Outline each blood parasite and name the species.
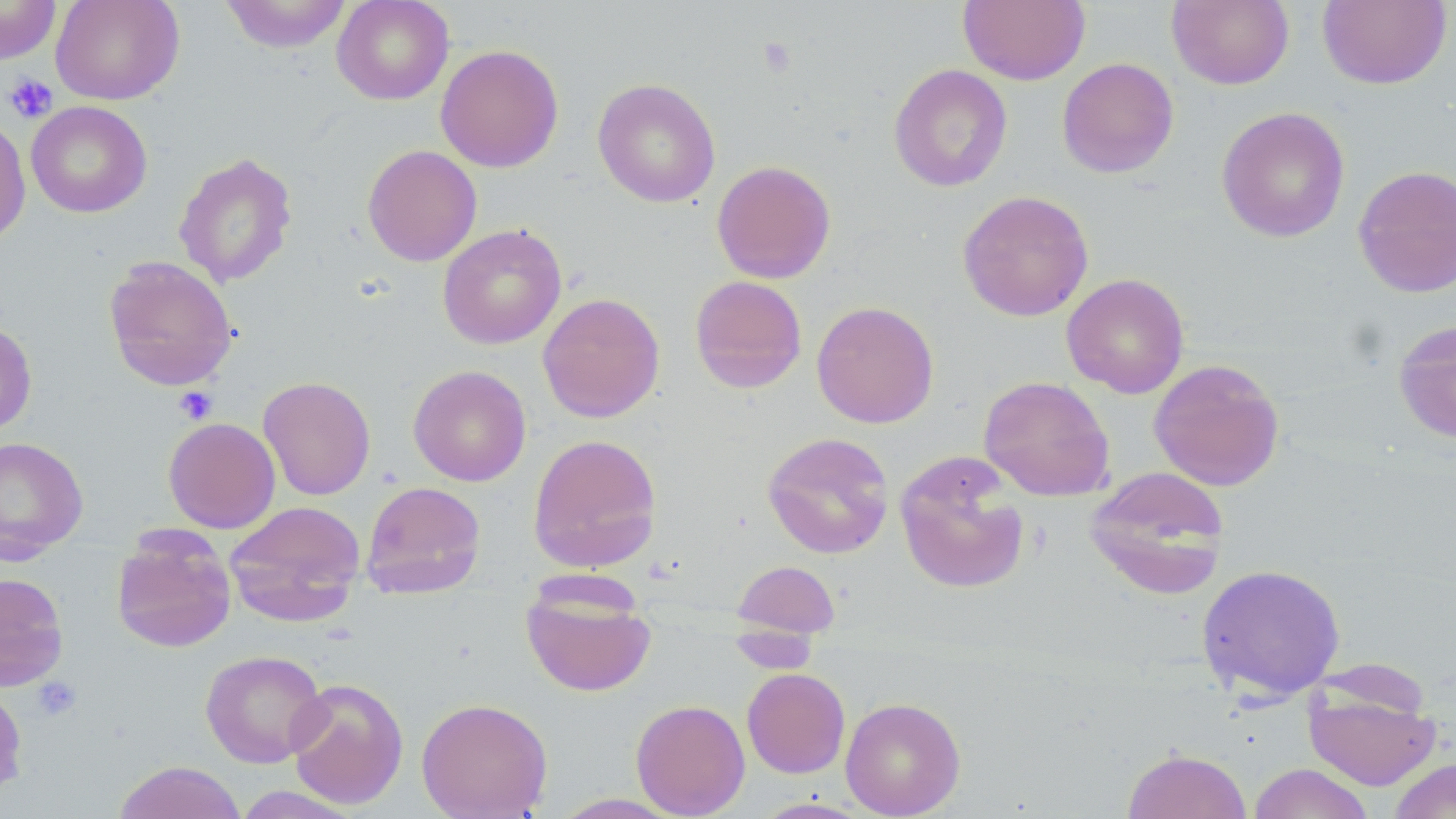
No blood parasites observed.

Approximate bounding boxes as (x1, y1, x2, y2) in pixels. Uninfected red blood cell locations: (0, 0, 62, 65), (50, 0, 184, 105), (220, 0, 353, 53), (332, 0, 454, 105), (958, 0, 1090, 86), (1318, 0, 1451, 89), (1167, 1, 1294, 90), (435, 44, 564, 172), (1056, 57, 1179, 179), (888, 64, 1013, 192), (592, 78, 721, 207), (26, 100, 152, 218), (1216, 106, 1350, 243), (0, 113, 31, 249), (362, 144, 483, 267), (173, 152, 298, 288), (711, 160, 836, 284), (1352, 165, 1456, 298), (957, 190, 1094, 322), (438, 224, 566, 349), (103, 256, 238, 392), (1062, 273, 1189, 399), (689, 275, 808, 393), (537, 292, 665, 423), (811, 301, 939, 428), (0, 319, 37, 437), (1393, 319, 1456, 444), (1148, 358, 1285, 491), (408, 365, 531, 487), (258, 375, 376, 501), (978, 376, 1115, 501), (163, 417, 280, 533), (762, 432, 895, 559), (527, 433, 662, 573), (0, 437, 89, 564), (895, 453, 1030, 595), (1086, 467, 1231, 600), (360, 480, 486, 599), (225, 500, 366, 625), (111, 528, 236, 653), (733, 560, 840, 638), (1196, 563, 1345, 701), (0, 572, 69, 691), (520, 578, 656, 697), (729, 635, 820, 671), (200, 649, 328, 768), (742, 668, 850, 778), (286, 677, 409, 810), (0, 681, 28, 800), (1304, 684, 1440, 790), (415, 696, 553, 819), (840, 696, 966, 818), (631, 699, 750, 818), (1121, 747, 1252, 819), (1388, 758, 1456, 819), (113, 760, 247, 819), (1248, 763, 1375, 819), (231, 785, 363, 818), (548, 793, 686, 818). Platelet locations: (757, 37, 798, 78), (3, 72, 58, 124), (173, 386, 217, 424), (31, 676, 81, 722). Slide-level diagnosis: no evidence of blood parasites. May-Grünwald-Giemsa stain. Optical microscopy. Thin blood film. Image is 1456×819 pixels. Single field of view. Captured at 1000x magnification.